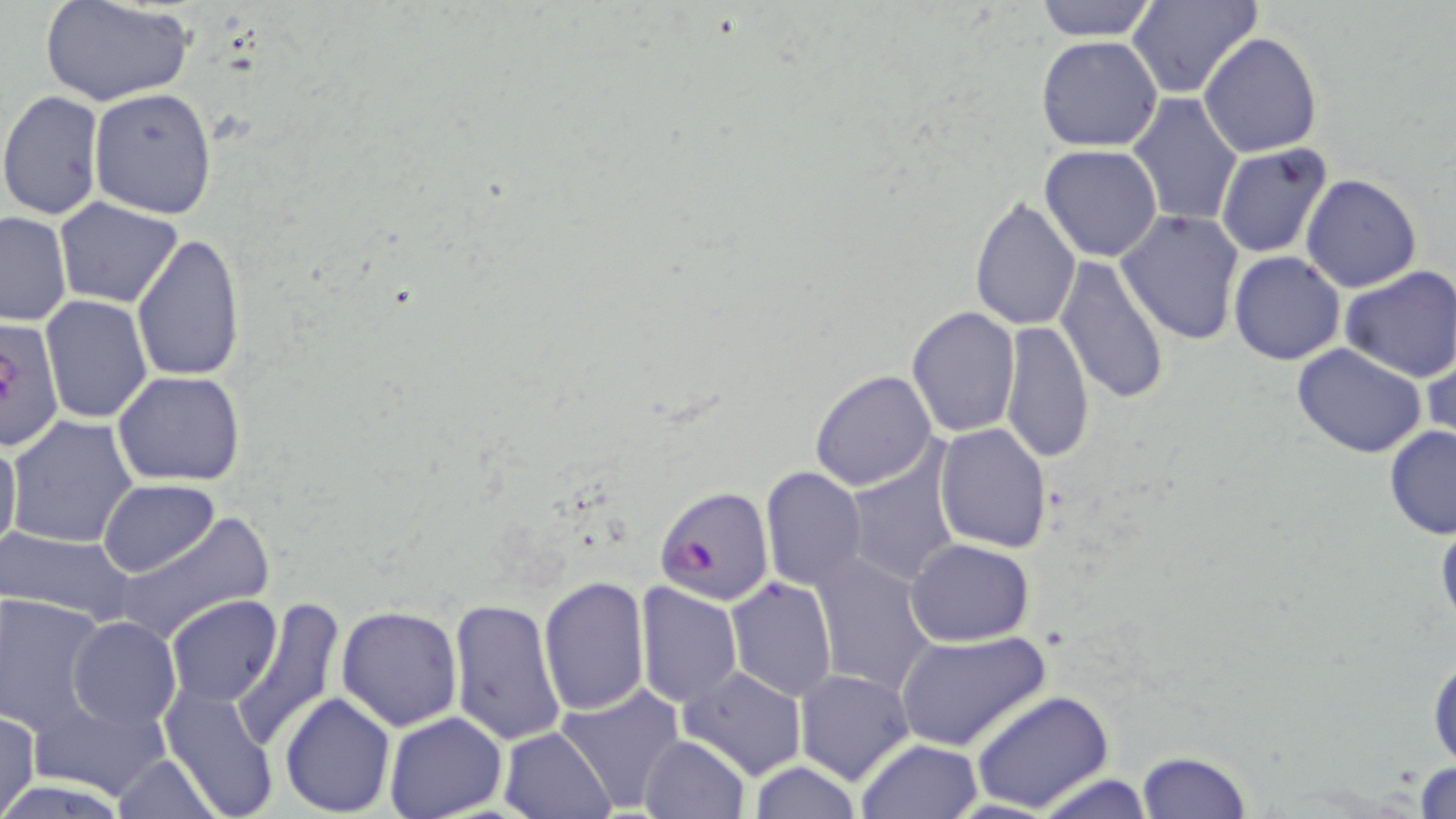
slide-level diagnosis = Plasmodium falciparum
modality = light microscopy
preparation = thin blood smear
field of view = single
uninfected red blood cell locations = approximate bounding boxes as [x1, y1, x2, y2] in pixels: [43, 0, 194, 108], [1032, 0, 1160, 41], [1128, 0, 1261, 99], [1198, 31, 1324, 158], [1036, 36, 1163, 151], [89, 87, 218, 217], [0, 90, 104, 219], [1127, 93, 1244, 227], [1039, 144, 1162, 261], [1215, 144, 1334, 259], [1299, 173, 1423, 293], [969, 195, 1081, 329], [55, 198, 182, 307], [1116, 209, 1245, 345], [0, 212, 72, 326], [131, 232, 245, 384], [1229, 251, 1345, 364], [1055, 254, 1173, 405], [1337, 265, 1455, 382], [40, 296, 153, 424], [907, 307, 1020, 437], [1000, 321, 1096, 466], [1421, 339, 1455, 452], [1292, 344, 1427, 459], [810, 369, 936, 491], [112, 371, 245, 488], [7, 413, 137, 546], [933, 424, 1053, 552], [1382, 426, 1455, 540], [0, 435, 22, 561], [845, 451, 960, 586], [759, 466, 869, 591], [99, 479, 219, 578], [115, 514, 273, 646], [1435, 514, 1456, 631], [0, 528, 136, 628], [905, 539, 1034, 646], [810, 551, 937, 696], [537, 575, 649, 715], [725, 577, 837, 701], [635, 582, 743, 708], [1, 593, 106, 733], [166, 595, 283, 707], [231, 598, 344, 749], [446, 598, 564, 745], [336, 605, 463, 730], [67, 617, 181, 730], [896, 629, 1051, 753], [1427, 645, 1455, 769], [678, 666, 807, 779], [795, 669, 915, 785], [159, 685, 282, 819], [557, 685, 685, 813], [970, 690, 1115, 813], [280, 692, 395, 814], [26, 695, 172, 802], [0, 708, 41, 818], [383, 710, 507, 819], [498, 727, 616, 819], [638, 735, 751, 819], [855, 738, 983, 819], [1136, 750, 1251, 818], [115, 755, 220, 818], [1412, 759, 1456, 816], [748, 762, 860, 818], [1030, 771, 1158, 818]
magnification = 1000x
Plasmodium falciparum-infected red blood cell locations = approximate bounding boxes as [x1, y1, x2, y2] in pixels: [0, 314, 65, 458], [657, 484, 774, 604]
image size = 1456×819 pixels
stain = May-Grünwald-Giemsa